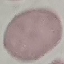

{
  "result": "no malaria parasites detected",
  "image_type": "automatically extracted cell patch, resized to 64 × 64 pixels",
  "preparation": "thin blood film",
  "stain": "Giemsa",
  "capture": "smartphone through the microscope eyepiece"
}